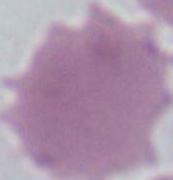
magnification = 1000x
modality = photomicrograph
identification = red blood cell